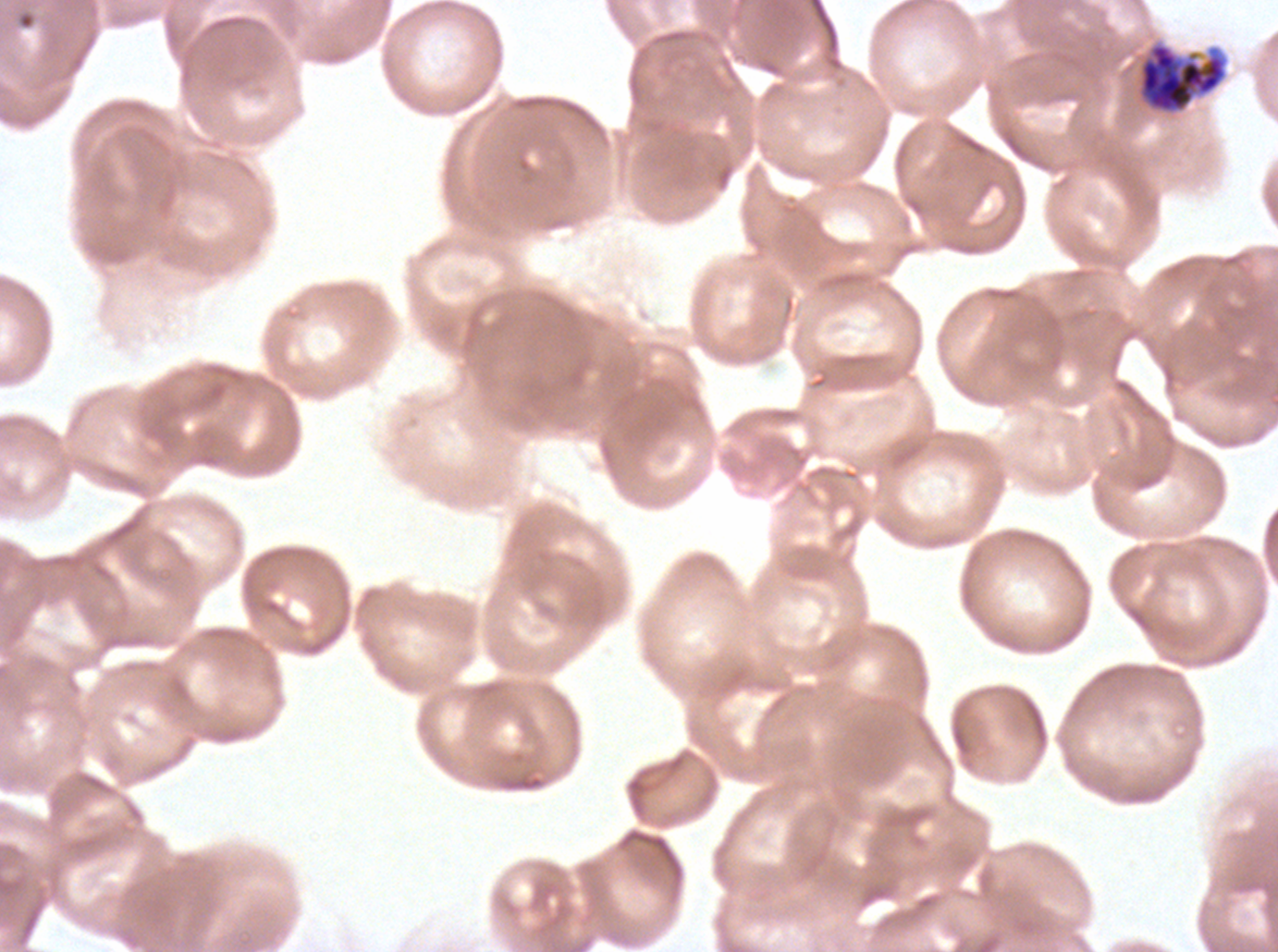
Approximate bounding boxes as (x1, y1, x2, y2) in pixels.
Summary:
  - Early schizont locations: (1139, 43, 1225, 113)
  - Ring locations: (15, 8, 38, 31)
  - Preparation: thin blood film
  - Specimen: ex-vivo P. falciparum culture from a patient in The Gambia, grown for 24 to 48 hours
  - Field of view: sub-image separated from a larger composite
  - Stain: Giemsa
  - Image size: 1278×952 pixels
  - Life-cycle stages observed: ring, early schizont